Outline each blood parasite and name the species.
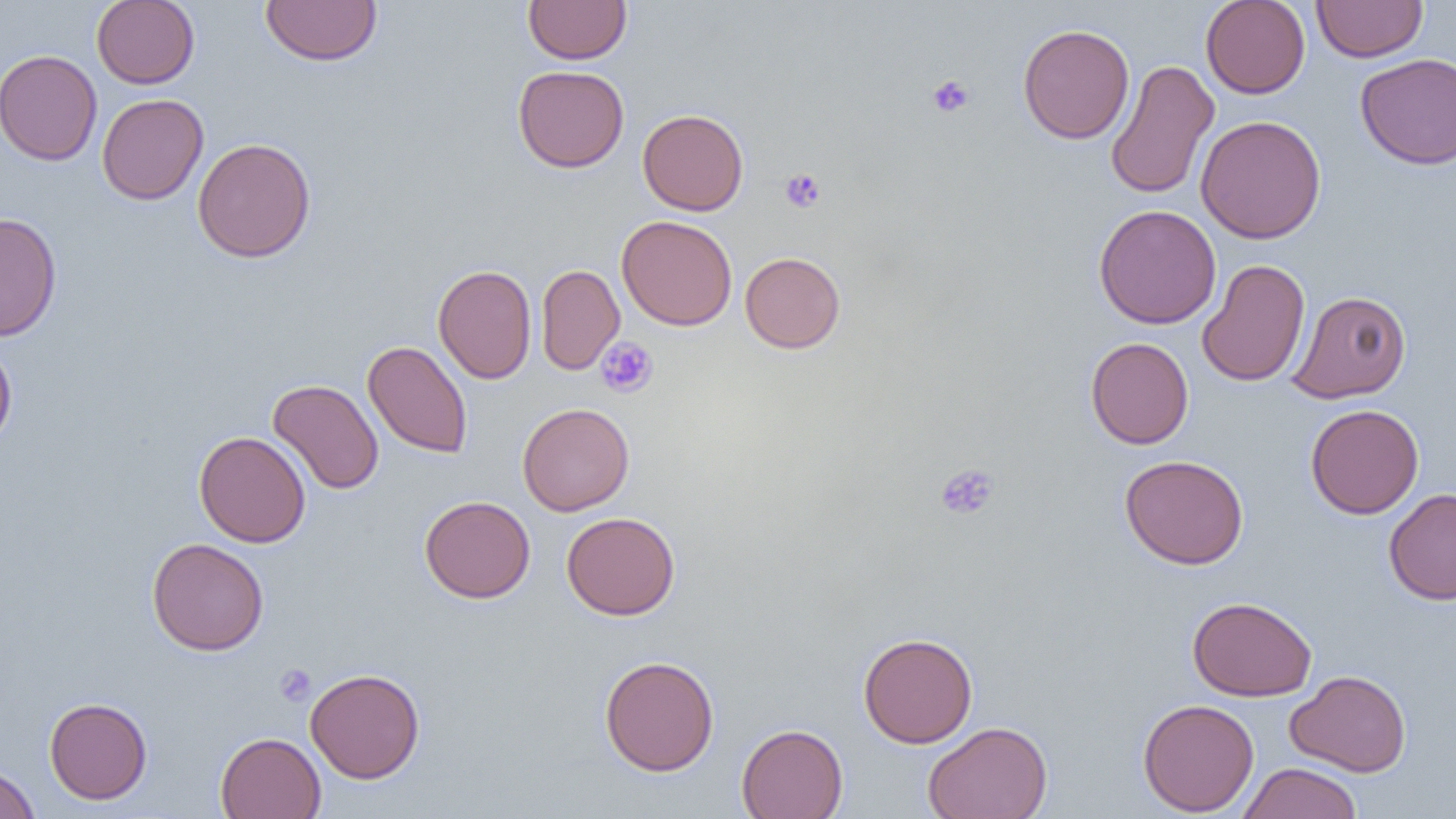

No blood parasites observed.

slide_level_diagnosis: negative for blood parasites
image_size: 1456×819 pixels
magnification: 1000x
uninfected_red_blood_cell_locations: 'approximate bounding boxes as named x1/y1/x2/y2 corners in pixels: (x1=91, y1=0, x2=200, y2=89), (x1=260, y1=0, x2=382, y2=66), (x1=523, y1=0, x2=632, y2=65), (x1=1200, y1=0, x2=1310, y2=99), (x1=1311, y1=0, x2=1428, y2=62), (x1=1017, y1=23, x2=1134, y2=144), (x1=0, y1=49, x2=102, y2=166), (x1=1355, y1=52, x2=1456, y2=170), (x1=1105, y1=59, x2=1219, y2=200), (x1=513, y1=65, x2=629, y2=173), (x1=97, y1=93, x2=209, y2=205), (x1=637, y1=108, x2=749, y2=216), (x1=1195, y1=115, x2=1327, y2=244), (x1=192, y1=137, x2=316, y2=263), (x1=1094, y1=204, x2=1221, y2=329), (x1=0, y1=212, x2=63, y2=341), (x1=616, y1=214, x2=738, y2=331), (x1=740, y1=252, x2=846, y2=353), (x1=1196, y1=259, x2=1311, y2=387), (x1=433, y1=264, x2=536, y2=384), (x1=536, y1=264, x2=625, y2=375), (x1=1288, y1=290, x2=1411, y2=403), (x1=1085, y1=336, x2=1194, y2=449), (x1=0, y1=339, x2=17, y2=449), (x1=362, y1=340, x2=473, y2=459), (x1=268, y1=379, x2=384, y2=494), (x1=518, y1=402, x2=635, y2=516), (x1=1305, y1=404, x2=1424, y2=519), (x1=194, y1=431, x2=311, y2=548), (x1=1120, y1=454, x2=1249, y2=570), (x1=1383, y1=488, x2=1456, y2=605), (x1=420, y1=495, x2=536, y2=603), (x1=562, y1=511, x2=680, y2=620), (x1=147, y1=537, x2=269, y2=655), (x1=1187, y1=596, x2=1317, y2=701), (x1=858, y1=632, x2=978, y2=748), (x1=599, y1=655, x2=720, y2=776), (x1=305, y1=667, x2=425, y2=783), (x1=1285, y1=669, x2=1412, y2=777), (x1=44, y1=696, x2=152, y2=804), (x1=1137, y1=698, x2=1259, y2=817), (x1=923, y1=721, x2=1053, y2=819), (x1=736, y1=723, x2=848, y2=819), (x1=215, y1=732, x2=326, y2=819), (x1=1237, y1=762, x2=1362, y2=819), (x1=0, y1=763, x2=40, y2=819)'
platelet_locations: 'approximate bounding boxes as named x1/y1/x2/y2 corners in pixels: (x1=926, y1=74, x2=975, y2=118), (x1=780, y1=168, x2=826, y2=213), (x1=595, y1=337, x2=658, y2=398), (x1=935, y1=463, x2=1000, y2=520), (x1=274, y1=664, x2=316, y2=705)'
preparation: thin blood smear
field_of_view: single
modality: optical microscopy